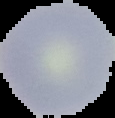

image_size: 115×118 pixels
malaria_status: uninfected
image_type: segmented cell region with the area outside set to black
preparation: thin blood smear